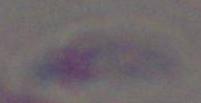

Toxoplasma gondii is shown. Photomicrograph. 1000x magnification.